State which parasite is depicted.
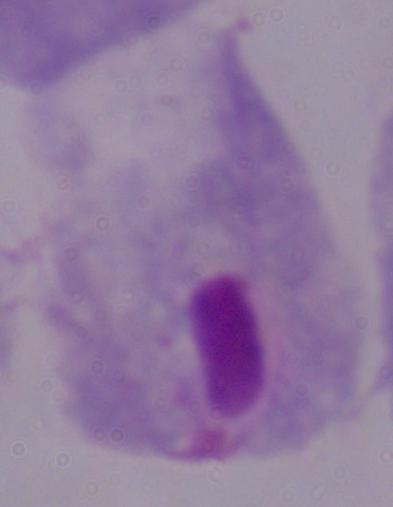

This is a trichomonad.

1000x magnification. Photomicrograph.